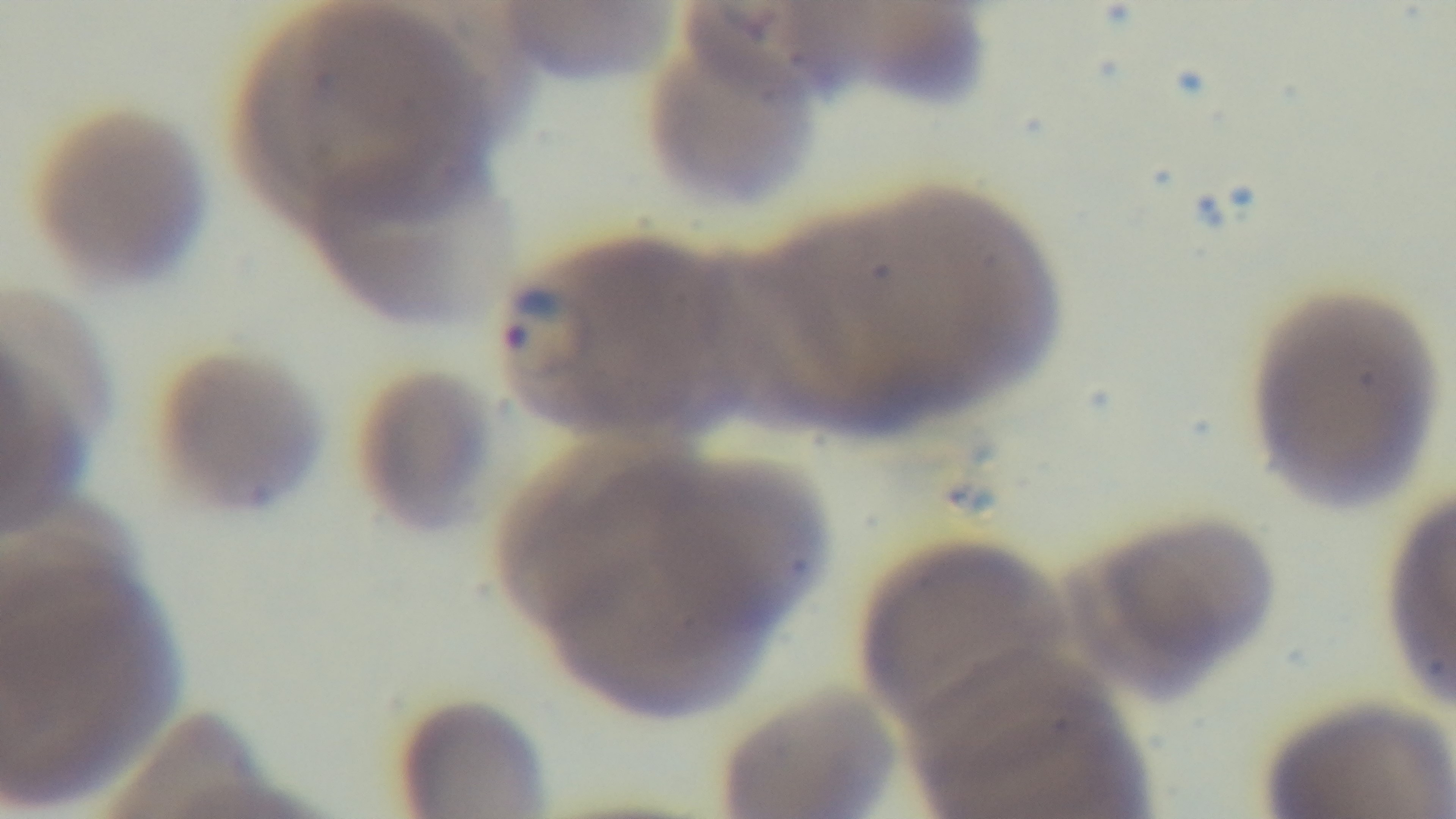 Single field of view. Photomicrograph. 100x oil-immersion objective. Malaria status: positive. Preparation: thin smear. Giemsa stain. Mounted 4K digital camera.